Assess this cell for malaria.
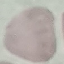

It is uninfected.

{
  "image_type": "cell patch, automatically extracted from a larger field of view and resized to 64 × 64 pixels",
  "preparation": "thin blood smear",
  "capture": "smartphone through the microscope eyepiece",
  "stain": "Giemsa"
}